Classify this cell by malaria status.
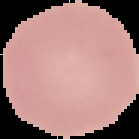

It is uninfected.

From a thin blood film. The area outside the segmented cell region is set to black. Image is 139×139 pixels.